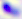
Summary:
  - Identification: Toxoplasma gondii
  - Modality: micrograph
  - Magnification: 400x